Assess for Plasmodium parasites.
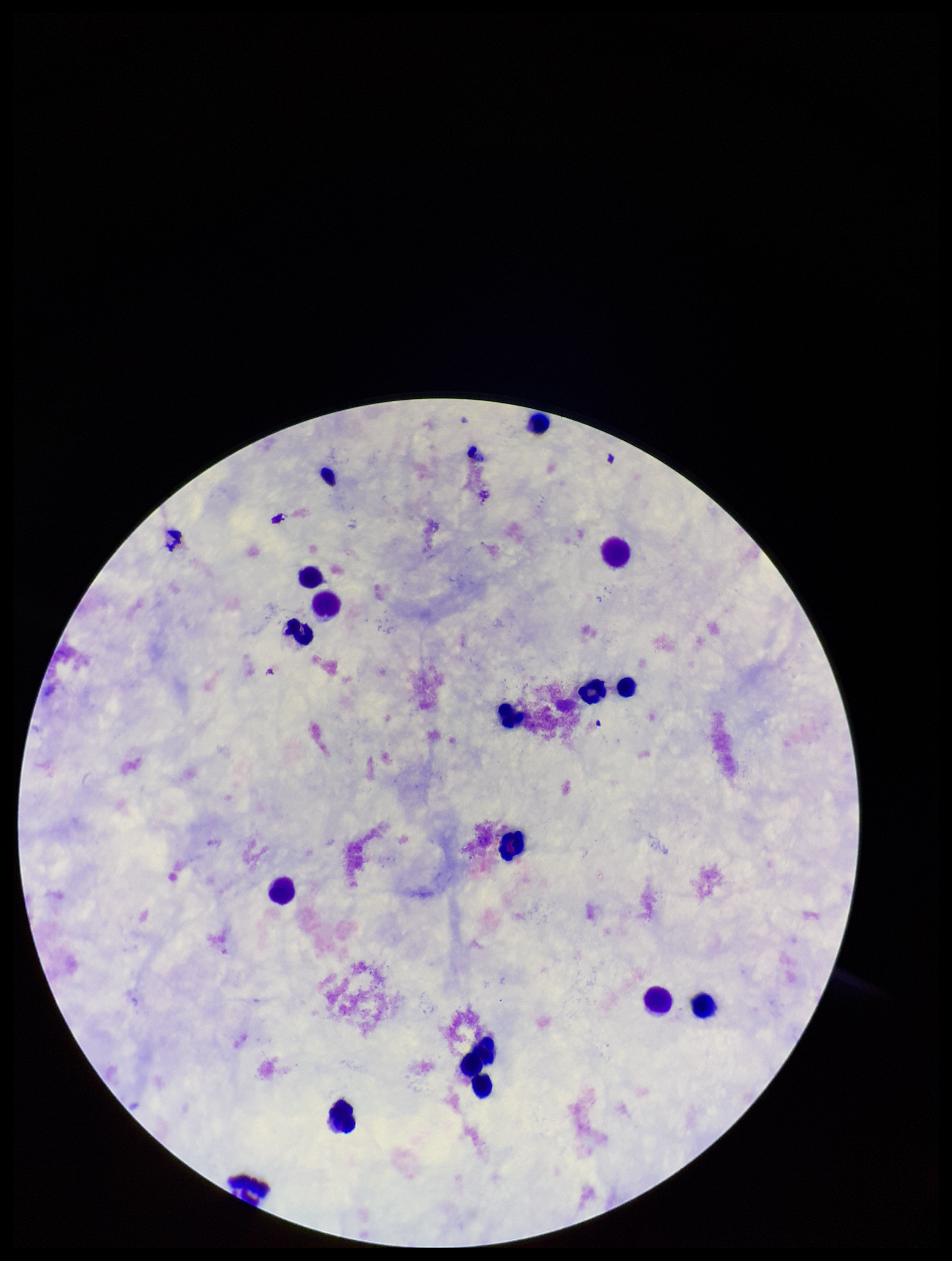
None seen.

field of view = single
patient malaria status = negative
preparation = thick blood smear
parasite count = 0
capture = smartphone photograph through the microscope eyepiece
leukocyte count = 16
stain = Giemsa
image size = 952×1261 pixels